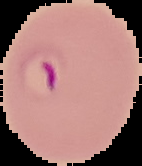

Summary:
  - Preparation: thin blood smear
  - Image type: segmented cell region on a black background
  - Malaria status: parasitized
  - Image size: 142×166 pixels